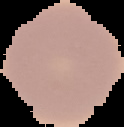

image type = segmented cell region with the area outside set to black
image size = 124×127 pixels
preparation = thin blood film
result = negative for Plasmodium parasites